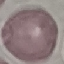
Result: no malaria parasites detected. Thin blood film. Giemsa-stained preparation. Cell patch, automatically extracted from a larger field of view and resized to 64 × 64 pixels. Photographed with a smartphone camera at the microscope eyepiece.